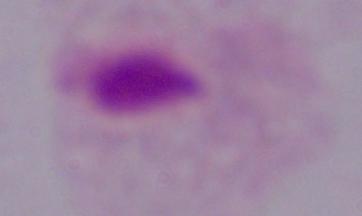
Summary:
  - Magnification: 1000x
  - Modality: photomicrograph
  - Identification: trichomonad